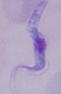
modality = photomicrograph
identification = trypanosome
magnification = 1000x